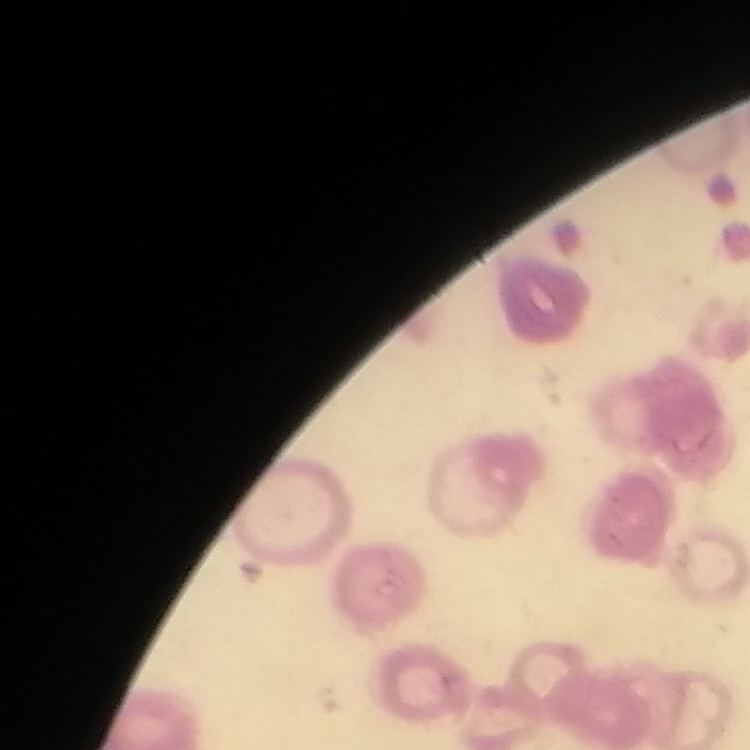

Summary:
  - Erythrocyte morphology: rouleaux formation
  - Stain: Field's or Giemsa
  - Preparation: thin blood smear
  - Image type: square crop of a larger photomicrograph